Assess this cell for malaria.
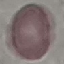
It is uninfected.

Summary:
  - Preparation: thin blood film
  - Stain: Giemsa
  - Image type: automatically extracted cell patch, resized to 64 × 64 pixels
  - Capture: smartphone through the microscope eyepiece